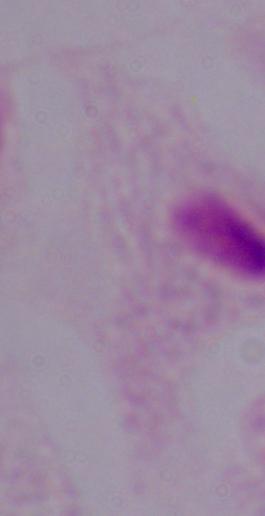

Photomicrograph. Captured at 1000x magnification. A trichomonad is seen.